Classify this cell by malaria status.
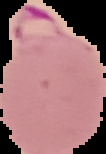

It is parasitized.

Segmented cell region on a black background. Image is 106×154 pixels. From a thin blood film.